State the preparation type.
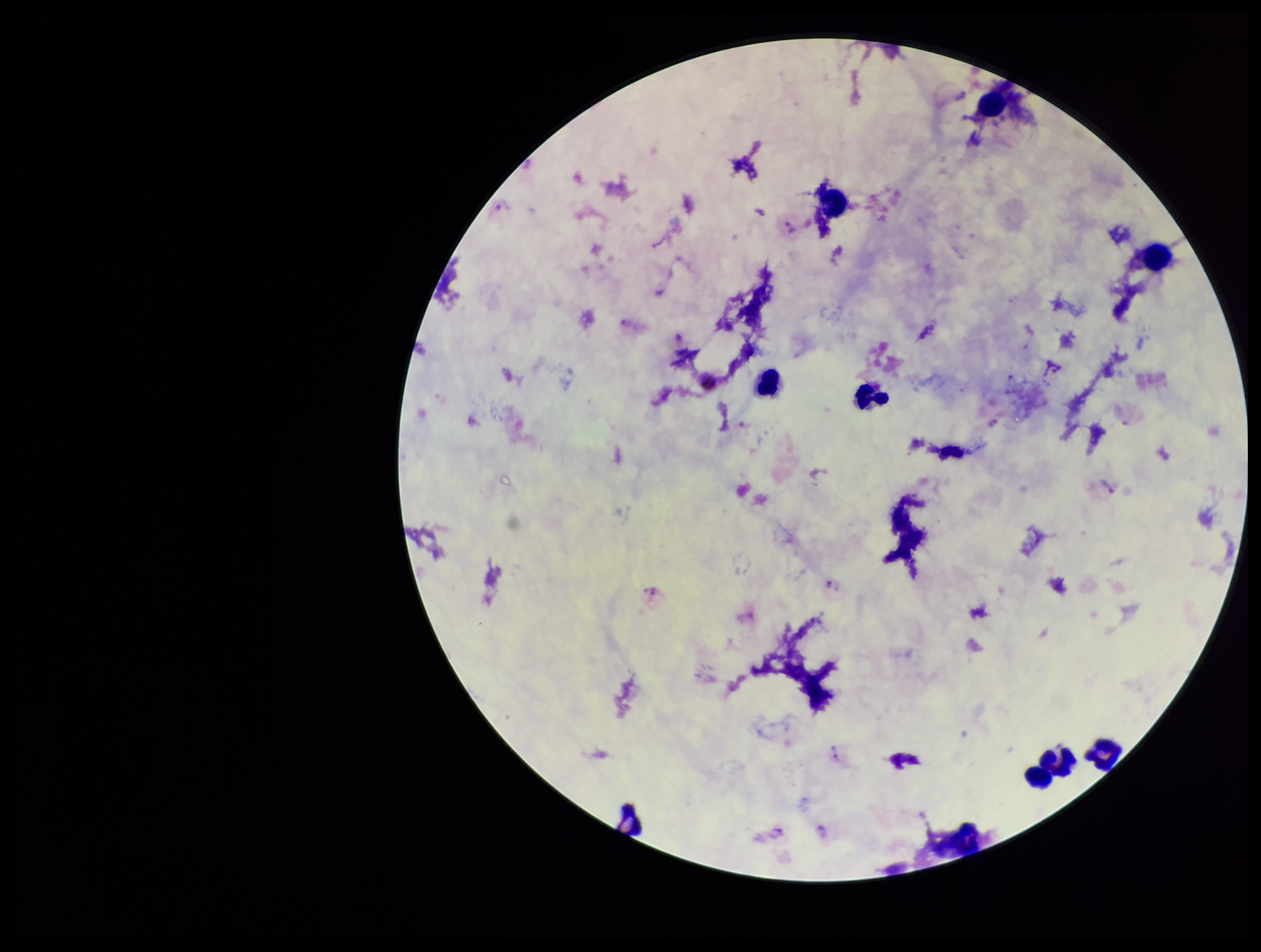
A thick smear.

Plasmodium parasites: seen. Single field of view. Parasite count: 6. Leukocyte count: 8. Image is 1261×952 pixels. Photographed through the microscope eyepiece with a smartphone camera. Species reported for this patient: Plasmodium vivax. Stained with Giemsa. Patient malaria status: infected.